Locate and identify every blood parasite.
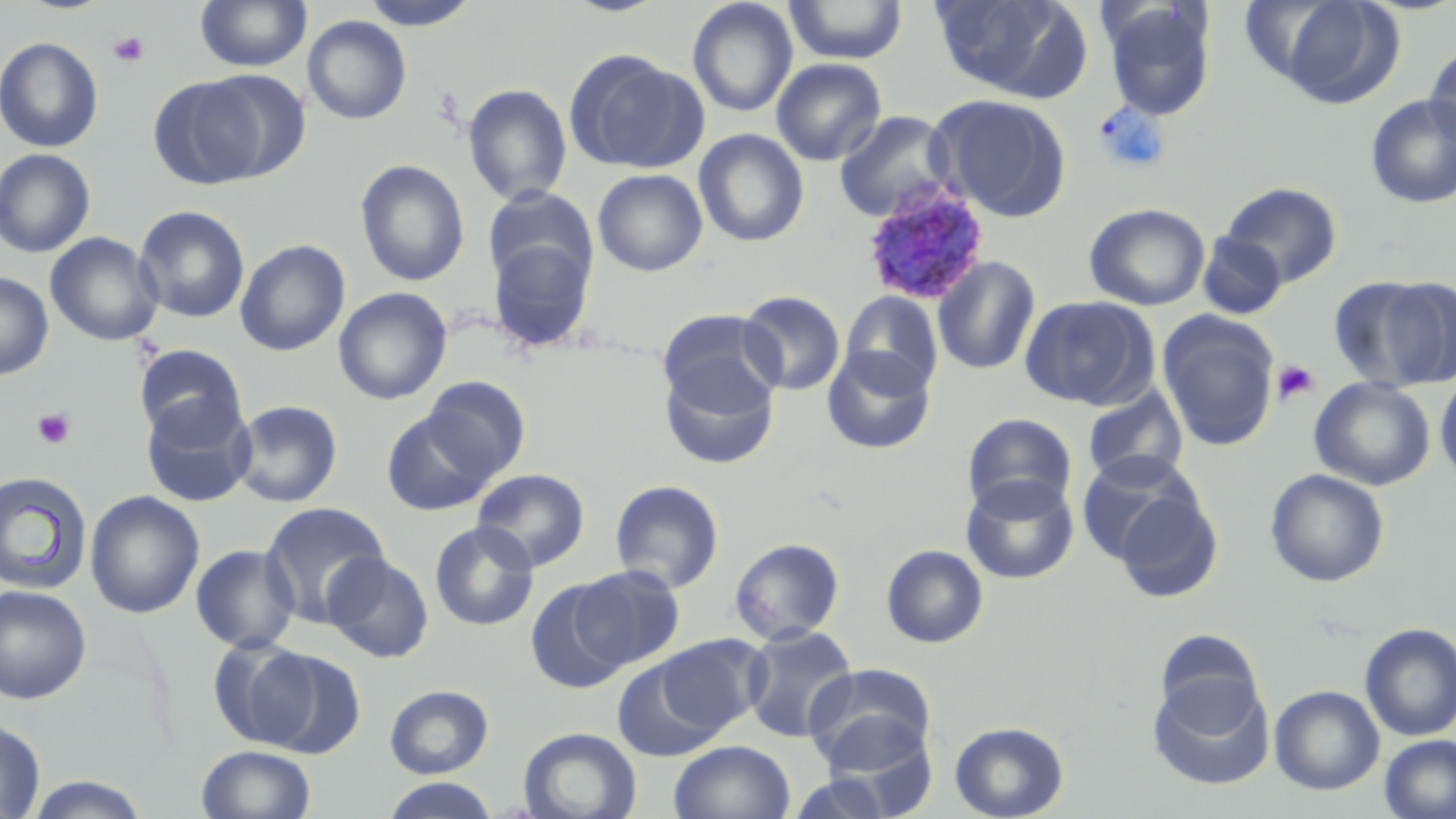
Approximate bounding boxes as named x1/y1/x2/y2 corners in pixels.
Plasmodium ovale-infected red blood cells: (x1=859, y1=181, x2=990, y2=307).
No Plasmodium falciparum, Plasmodium malariae, Plasmodium vivax, Babesia divergens, or Trypanosoma brucei observed.

slide-level diagnosis = Plasmodium ovale
modality = optical microscopy
uninfected red blood cell locations = approximate bounding boxes as named x1/y1/x2/y2 corners in pixels: (x1=194, y1=0, x2=312, y2=72), (x1=358, y1=0, x2=482, y2=30), (x1=564, y1=0, x2=669, y2=17), (x1=687, y1=0, x2=798, y2=117), (x1=783, y1=0, x2=909, y2=66), (x1=930, y1=0, x2=1092, y2=101), (x1=1275, y1=1, x2=1405, y2=107), (x1=1102, y1=3, x2=1216, y2=121), (x1=303, y1=15, x2=412, y2=124), (x1=0, y1=37, x2=103, y2=153), (x1=1424, y1=44, x2=1456, y2=149), (x1=564, y1=50, x2=703, y2=175), (x1=771, y1=57, x2=887, y2=166), (x1=198, y1=69, x2=312, y2=181), (x1=148, y1=75, x2=270, y2=189), (x1=462, y1=83, x2=573, y2=206), (x1=926, y1=94, x2=1071, y2=222), (x1=1365, y1=94, x2=1456, y2=209), (x1=834, y1=110, x2=955, y2=222), (x1=693, y1=128, x2=809, y2=247), (x1=0, y1=148, x2=96, y2=258), (x1=355, y1=159, x2=470, y2=287), (x1=592, y1=169, x2=708, y2=276), (x1=1220, y1=182, x2=1343, y2=287), (x1=482, y1=186, x2=597, y2=292), (x1=1084, y1=203, x2=1210, y2=311), (x1=134, y1=205, x2=250, y2=324), (x1=45, y1=232, x2=164, y2=346), (x1=1197, y1=233, x2=1286, y2=319), (x1=487, y1=236, x2=596, y2=353), (x1=235, y1=239, x2=351, y2=356), (x1=932, y1=255, x2=1041, y2=375), (x1=0, y1=271, x2=54, y2=380), (x1=1329, y1=275, x2=1455, y2=392), (x1=333, y1=287, x2=452, y2=405), (x1=736, y1=290, x2=845, y2=397), (x1=840, y1=292, x2=943, y2=397), (x1=1020, y1=295, x2=1156, y2=410), (x1=657, y1=309, x2=783, y2=414), (x1=1158, y1=312, x2=1280, y2=452), (x1=134, y1=343, x2=247, y2=441), (x1=822, y1=346, x2=936, y2=454), (x1=659, y1=356, x2=779, y2=470), (x1=1435, y1=371, x2=1456, y2=486), (x1=421, y1=375, x2=531, y2=482), (x1=1309, y1=377, x2=1435, y2=491), (x1=1082, y1=386, x2=1189, y2=486), (x1=140, y1=395, x2=257, y2=507), (x1=231, y1=399, x2=343, y2=507), (x1=380, y1=409, x2=500, y2=516), (x1=962, y1=413, x2=1078, y2=517), (x1=1077, y1=451, x2=1205, y2=569), (x1=472, y1=468, x2=590, y2=571), (x1=1265, y1=468, x2=1389, y2=587), (x1=0, y1=471, x2=94, y2=596), (x1=961, y1=475, x2=1079, y2=585), (x1=609, y1=479, x2=725, y2=594), (x1=1111, y1=488, x2=1224, y2=603), (x1=84, y1=490, x2=205, y2=619), (x1=260, y1=501, x2=392, y2=627), (x1=429, y1=521, x2=539, y2=632), (x1=729, y1=537, x2=845, y2=645), (x1=190, y1=543, x2=300, y2=654), (x1=881, y1=544, x2=988, y2=648), (x1=323, y1=552, x2=435, y2=663), (x1=571, y1=565, x2=685, y2=669), (x1=526, y1=579, x2=632, y2=693), (x1=0, y1=585, x2=92, y2=704), (x1=1359, y1=623, x2=1456, y2=742), (x1=741, y1=625, x2=858, y2=742), (x1=1152, y1=631, x2=1263, y2=724), (x1=655, y1=634, x2=768, y2=736), (x1=207, y1=636, x2=319, y2=749), (x1=252, y1=648, x2=367, y2=759), (x1=611, y1=655, x2=728, y2=763), (x1=804, y1=663, x2=937, y2=771), (x1=1147, y1=676, x2=1274, y2=790), (x1=384, y1=684, x2=494, y2=778), (x1=1269, y1=685, x2=1384, y2=795), (x1=0, y1=717, x2=46, y2=818), (x1=949, y1=721, x2=1069, y2=819), (x1=518, y1=726, x2=642, y2=819), (x1=1379, y1=734, x2=1456, y2=819), (x1=669, y1=740, x2=795, y2=819), (x1=196, y1=745, x2=317, y2=819), (x1=789, y1=770, x2=895, y2=819), (x1=23, y1=774, x2=150, y2=818), (x1=381, y1=778, x2=498, y2=819)
stain = May-Grünwald-Giemsa
image size = 1456×819 pixels
preparation = thin blood smear
platelet locations = approximate bounding boxes as named x1/y1/x2/y2 corners in pixels: (x1=108, y1=31, x2=150, y2=67), (x1=1273, y1=359, x2=1320, y2=405), (x1=32, y1=408, x2=76, y2=449)
magnification = 1000x
field of view = one of a larger specimen